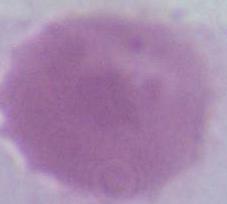 1000x magnification. Micrograph. An erythrocyte is seen.